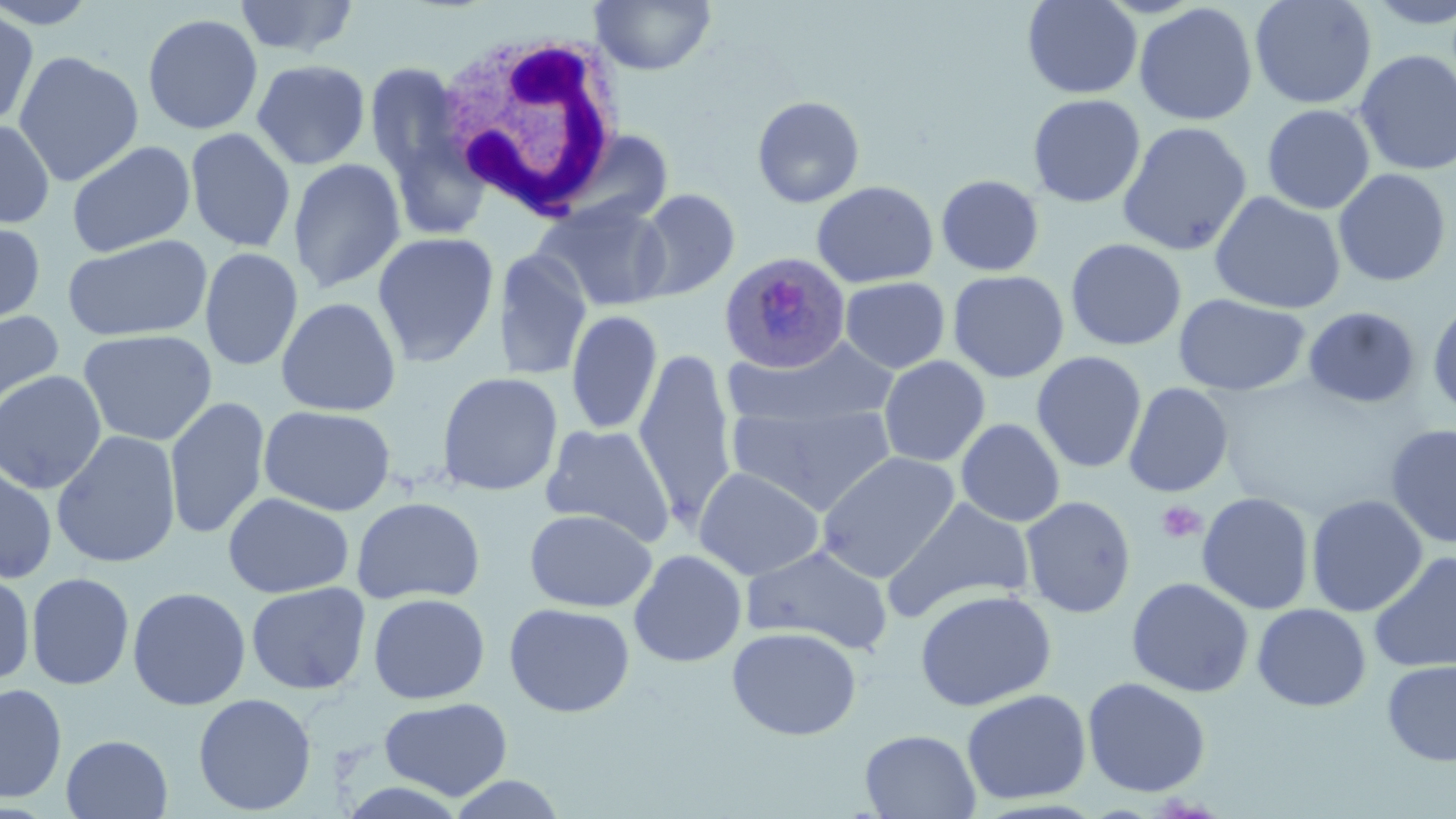
Approximate bounding boxes as named x1/y1/x2/y2 corners in pixels. Uninfected red blood cell locations: (x1=232, y1=0, x2=362, y2=59), (x1=590, y1=0, x2=717, y2=76), (x1=1022, y1=0, x2=1142, y2=99), (x1=1249, y1=0, x2=1377, y2=110), (x1=1361, y1=0, x2=1456, y2=28), (x1=1134, y1=3, x2=1258, y2=126), (x1=0, y1=8, x2=40, y2=131), (x1=141, y1=12, x2=264, y2=135), (x1=13, y1=50, x2=144, y2=186), (x1=1355, y1=50, x2=1456, y2=176), (x1=251, y1=58, x2=371, y2=170), (x1=364, y1=61, x2=466, y2=183), (x1=1027, y1=94, x2=1146, y2=208), (x1=751, y1=95, x2=866, y2=208), (x1=1262, y1=104, x2=1375, y2=214), (x1=0, y1=118, x2=56, y2=230), (x1=1117, y1=121, x2=1252, y2=256), (x1=184, y1=127, x2=296, y2=253), (x1=384, y1=130, x2=492, y2=245), (x1=66, y1=140, x2=196, y2=257), (x1=287, y1=157, x2=406, y2=294), (x1=1333, y1=168, x2=1452, y2=287), (x1=936, y1=174, x2=1045, y2=276), (x1=811, y1=180, x2=938, y2=288), (x1=632, y1=188, x2=740, y2=301), (x1=1209, y1=191, x2=1346, y2=314), (x1=535, y1=199, x2=672, y2=311), (x1=552, y1=199, x2=666, y2=431), (x1=0, y1=219, x2=46, y2=328), (x1=372, y1=231, x2=500, y2=367), (x1=61, y1=233, x2=213, y2=343), (x1=1065, y1=238, x2=1186, y2=351), (x1=199, y1=247, x2=303, y2=372), (x1=494, y1=249, x2=592, y2=382), (x1=947, y1=270, x2=1069, y2=383), (x1=839, y1=277, x2=950, y2=373), (x1=1173, y1=293, x2=1310, y2=396), (x1=275, y1=295, x2=402, y2=417), (x1=1427, y1=300, x2=1456, y2=419), (x1=1303, y1=306, x2=1421, y2=409), (x1=0, y1=309, x2=65, y2=418), (x1=565, y1=309, x2=663, y2=436), (x1=77, y1=328, x2=217, y2=446), (x1=726, y1=337, x2=898, y2=430), (x1=634, y1=348, x2=737, y2=525), (x1=1032, y1=351, x2=1147, y2=473), (x1=878, y1=356, x2=990, y2=467), (x1=0, y1=369, x2=107, y2=494), (x1=435, y1=371, x2=564, y2=496), (x1=1123, y1=382, x2=1233, y2=498), (x1=164, y1=395, x2=270, y2=540), (x1=728, y1=401, x2=897, y2=515), (x1=258, y1=404, x2=396, y2=516), (x1=956, y1=417, x2=1066, y2=527), (x1=539, y1=423, x2=676, y2=546), (x1=1385, y1=423, x2=1456, y2=548), (x1=51, y1=429, x2=181, y2=568), (x1=816, y1=451, x2=961, y2=582), (x1=0, y1=461, x2=59, y2=585), (x1=693, y1=466, x2=826, y2=580), (x1=223, y1=491, x2=354, y2=598), (x1=1196, y1=492, x2=1315, y2=615), (x1=1306, y1=494, x2=1428, y2=617), (x1=1020, y1=495, x2=1136, y2=618), (x1=351, y1=496, x2=485, y2=605), (x1=883, y1=496, x2=1034, y2=622), (x1=524, y1=507, x2=657, y2=611), (x1=741, y1=544, x2=894, y2=654), (x1=628, y1=549, x2=747, y2=667), (x1=1368, y1=550, x2=1456, y2=674), (x1=0, y1=568, x2=35, y2=684), (x1=25, y1=572, x2=135, y2=690), (x1=1126, y1=577, x2=1254, y2=698), (x1=246, y1=581, x2=371, y2=695), (x1=127, y1=586, x2=251, y2=710), (x1=915, y1=588, x2=1056, y2=711), (x1=367, y1=592, x2=491, y2=704), (x1=503, y1=601, x2=636, y2=718), (x1=1252, y1=603, x2=1372, y2=712), (x1=726, y1=625, x2=862, y2=740), (x1=1382, y1=660, x2=1456, y2=766), (x1=1082, y1=676, x2=1212, y2=797), (x1=0, y1=682, x2=67, y2=803), (x1=961, y1=688, x2=1092, y2=805), (x1=192, y1=692, x2=317, y2=815), (x1=379, y1=696, x2=513, y2=800), (x1=860, y1=729, x2=981, y2=818), (x1=60, y1=734, x2=173, y2=819), (x1=444, y1=774, x2=570, y2=818). Plasmodium ovale-infected red blood cell locations: (x1=719, y1=252, x2=852, y2=373). White blood cell locations: (x1=433, y1=25, x2=628, y2=221). Platelet locations: (x1=1156, y1=500, x2=1207, y2=544). Slide-level diagnosis: Plasmodium ovale. May-Grünwald-Giemsa-stained preparation. Image is 1456×819 pixels. Optical microscopy. Single field of view. 1000x magnification. Thin blood film.